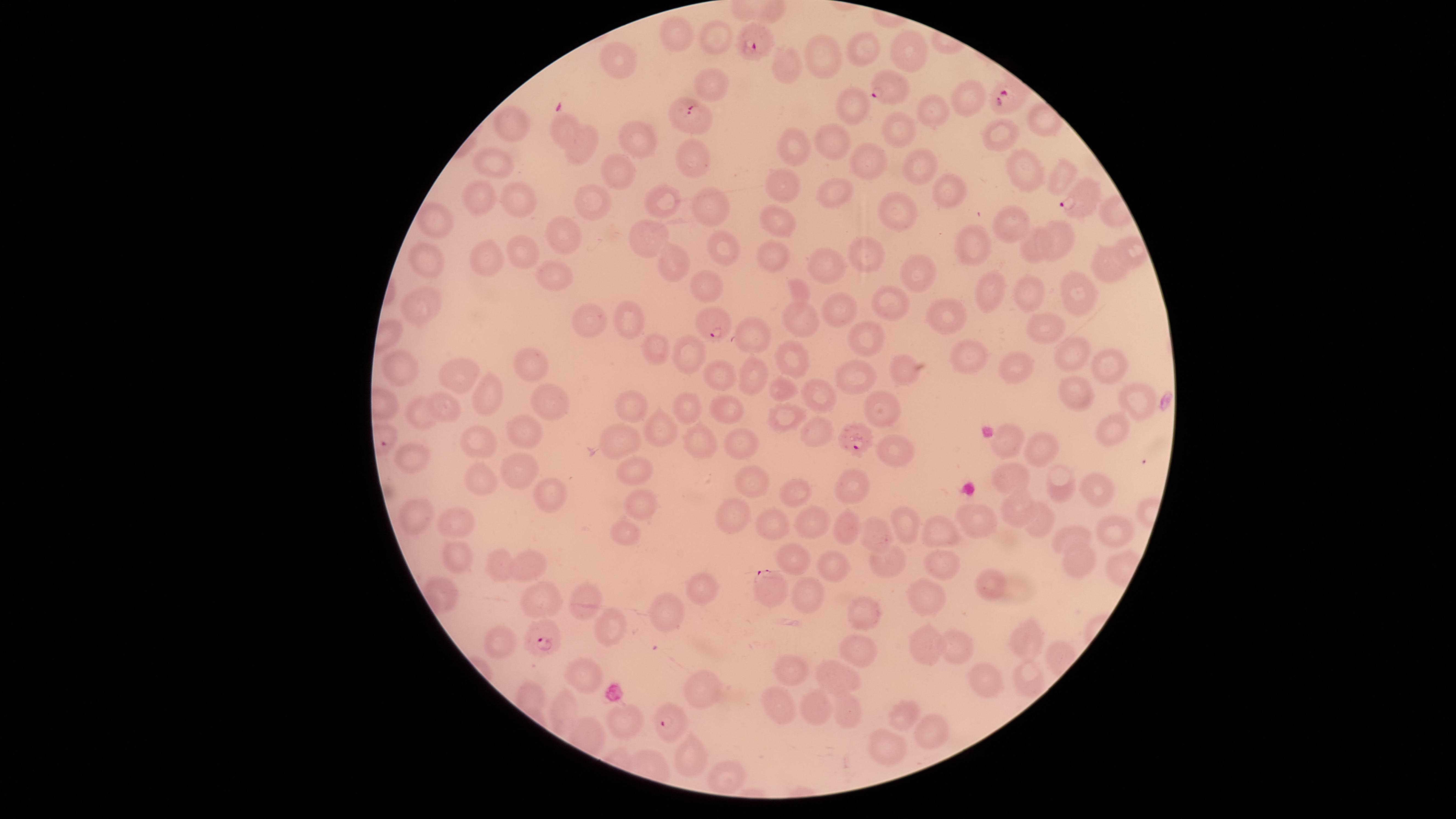

presence = malaria parasites identified
capture = smartphone photograph through the microscope eyepiece
preparation = thin blood film
parasitized red blood cells = approximate marker points, in pixels from the top-left corner: (x=756, y=41), (x=893, y=89), (x=1007, y=98), (x=691, y=117), (x=1077, y=200), (x=711, y=323), (x=859, y=437), (x=771, y=590), (x=546, y=637), (x=669, y=727)
image size = 1456×819 pixels
visible region = circular
field of view = single
species = Plasmodium falciparum
stain = Giemsa
uninfected red blood cells = approximate marker points, in pixels from the top-left corner: (x=675, y=33), (x=716, y=37), (x=863, y=46), (x=911, y=55), (x=822, y=57), (x=619, y=61), (x=786, y=72), (x=714, y=84), (x=970, y=97), (x=852, y=108), (x=932, y=113), (x=517, y=126), (x=559, y=130), (x=894, y=133), (x=642, y=135), (x=994, y=138), (x=833, y=140), (x=588, y=146), (x=790, y=146), (x=692, y=158), (x=867, y=160), (x=501, y=163), (x=917, y=166), (x=618, y=168), (x=1019, y=168), (x=1061, y=180), (x=835, y=185), (x=953, y=189), (x=781, y=190), (x=523, y=194), (x=588, y=198), (x=703, y=199), (x=662, y=200), (x=479, y=201), (x=896, y=211), (x=439, y=224), (x=1010, y=226), (x=776, y=227), (x=565, y=234), (x=1067, y=237), (x=654, y=242), (x=974, y=243), (x=1040, y=245), (x=1130, y=246), (x=726, y=248), (x=870, y=252), (x=529, y=254), (x=773, y=254), (x=491, y=258), (x=429, y=261), (x=819, y=263), (x=677, y=264), (x=1109, y=265), (x=914, y=271), (x=559, y=277), (x=704, y=285), (x=1001, y=288), (x=803, y=290), (x=1081, y=291), (x=1034, y=294), (x=890, y=303), (x=422, y=308), (x=839, y=312), (x=948, y=316), (x=633, y=318), (x=806, y=320), (x=589, y=324), (x=1050, y=329), (x=756, y=336), (x=869, y=339), (x=659, y=344), (x=1068, y=353), (x=688, y=354), (x=975, y=357), (x=789, y=362), (x=1013, y=362), (x=1109, y=363), (x=535, y=368), (x=906, y=371), (x=400, y=372), (x=720, y=373), (x=855, y=374), (x=754, y=378), (x=459, y=380), (x=785, y=387), (x=820, y=393), (x=1080, y=393), (x=482, y=397), (x=552, y=400), (x=1134, y=400), (x=635, y=404), (x=444, y=409), (x=688, y=409), (x=728, y=409), (x=883, y=410), (x=419, y=415), (x=781, y=416), (x=529, y=427), (x=658, y=430), (x=816, y=433), (x=1111, y=434), (x=701, y=438), (x=1013, y=438), (x=478, y=439), (x=624, y=442), (x=744, y=445), (x=1037, y=449), (x=890, y=457), (x=411, y=462), (x=523, y=469), (x=634, y=473), (x=1001, y=477), (x=481, y=480), (x=748, y=484), (x=1067, y=486), (x=853, y=487), (x=792, y=492), (x=1093, y=495), (x=555, y=499), (x=1021, y=509), (x=418, y=511), (x=639, y=511), (x=1032, y=514), (x=735, y=517), (x=814, y=517), (x=456, y=521), (x=850, y=523), (x=983, y=523), (x=902, y=524), (x=774, y=525), (x=625, y=528), (x=1078, y=529), (x=944, y=530), (x=1109, y=533), (x=873, y=535), (x=450, y=553), (x=888, y=560), (x=788, y=561), (x=1081, y=563), (x=503, y=567), (x=530, y=567), (x=941, y=568), (x=835, y=569), (x=984, y=585), (x=698, y=588), (x=812, y=591), (x=542, y=595), (x=584, y=596), (x=923, y=596), (x=861, y=607), (x=668, y=619), (x=611, y=628), (x=1023, y=637), (x=505, y=640), (x=860, y=647), (x=929, y=649), (x=953, y=651), (x=790, y=666), (x=838, y=672), (x=981, y=675), (x=1019, y=676), (x=583, y=678), (x=698, y=690), (x=780, y=703), (x=562, y=705), (x=816, y=705), (x=908, y=709), (x=848, y=710), (x=930, y=733), (x=688, y=752), (x=883, y=753), (x=729, y=776)